Report the malaria status of this cell.
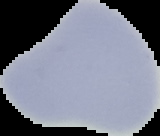
It is uninfected.

Image is 160×136 pixels. From a thin blood smear. The area outside the segmented cell region is set to black.